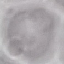

Summary:
  - Malaria status: uninfected
  - Stain: Giemsa
  - Capture: smartphone through the microscope eyepiece
  - Preparation: thin smear
  - Image type: cell patch, automatically extracted from a larger field of view and resized to 64 × 64 pixels